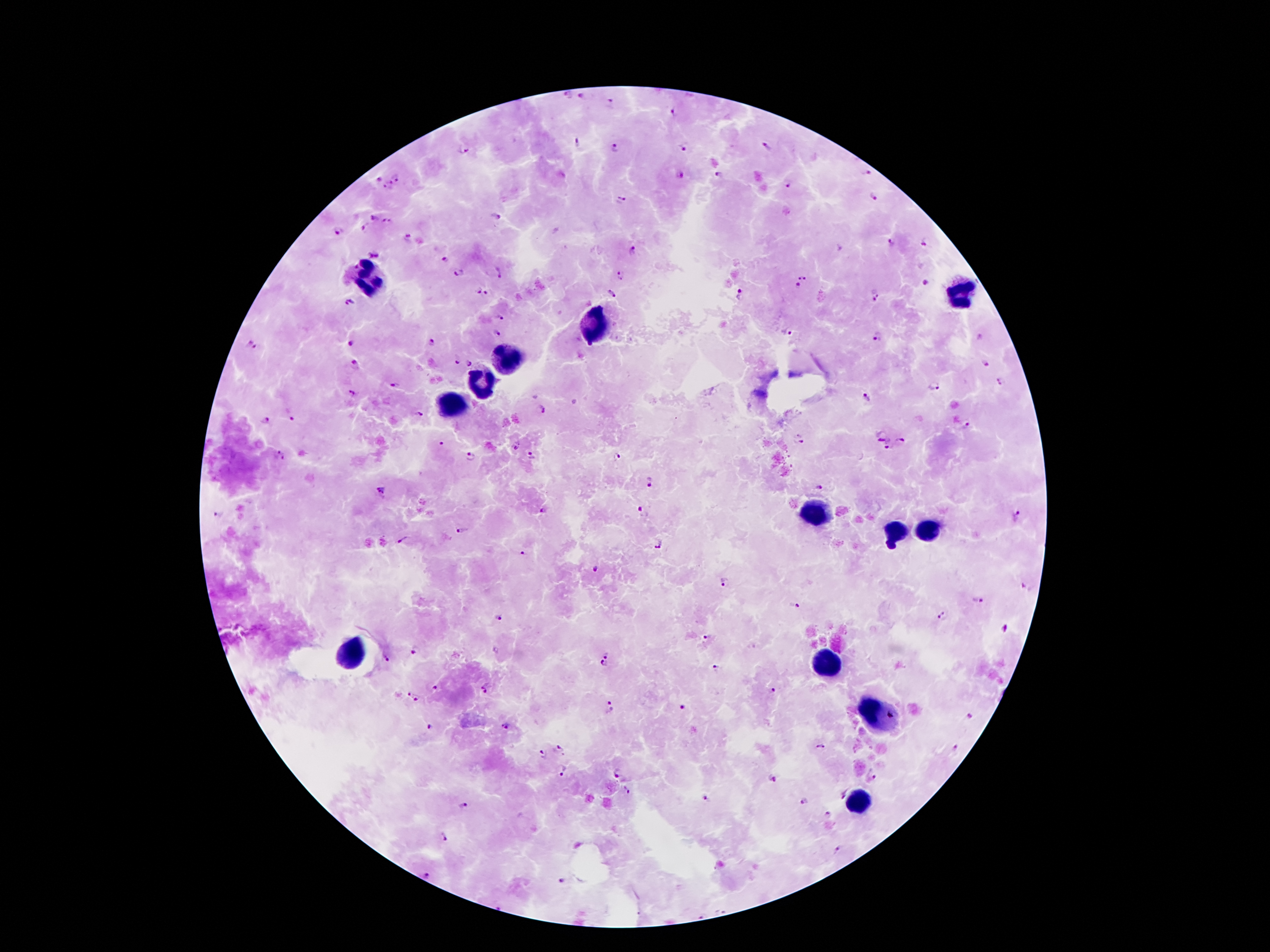 Approximate centers as [x, y] in pixels. Leukocyte locations: [372, 280], [960, 294], [592, 324], [508, 358], [480, 386], [450, 405], [816, 510], [895, 532], [932, 532], [347, 652], [829, 665], [876, 712], [859, 801]. Plasmodium parasite locations: [566, 96], [581, 97], [611, 104], [675, 114], [578, 143], [765, 146], [684, 147], [462, 149], [614, 150], [719, 173], [867, 173], [677, 176], [396, 178], [378, 179], [389, 183], [787, 185], [383, 188], [875, 197], [620, 201], [495, 217], [373, 218], [387, 221], [366, 229], [338, 231], [406, 239], [892, 243], [923, 243], [634, 249], [375, 256], [446, 261], [459, 271], [499, 271], [622, 275], [805, 276], [926, 282], [797, 284], [479, 291], [612, 292], [488, 293], [739, 293], [876, 297], [349, 303], [500, 317], [496, 332], [787, 332], [876, 335], [979, 338], [432, 341], [247, 342], [351, 343], [257, 348], [457, 359], [470, 363], [355, 364], [985, 364], [999, 381], [395, 386], [934, 386], [350, 393], [865, 397], [538, 409], [419, 414], [293, 419], [265, 420], [967, 423], [881, 435], [797, 438], [902, 440], [441, 445], [516, 446], [887, 447], [278, 450], [472, 455], [616, 456], [531, 457], [284, 458], [651, 480], [820, 487], [381, 490], [641, 509], [545, 510], [220, 514], [1015, 516], [465, 531], [403, 540], [660, 545], [523, 553], [596, 569], [726, 582], [1026, 588], [978, 599], [794, 606], [942, 615], [501, 618], [1005, 628], [706, 638], [415, 650], [608, 654], [386, 659], [605, 666], [717, 667], [437, 688], [487, 689], [774, 690], [410, 693], [417, 699], [611, 707], [681, 707], [969, 717], [430, 726], [505, 726], [821, 747], [954, 747], [559, 750], [542, 755], [562, 770], [618, 773], [874, 776], [772, 779], [627, 790], [840, 791], [705, 799], [805, 800], [464, 805], [828, 814], [443, 837], [840, 848], [425, 874], [562, 881]. Smartphone photograph taken through the microscope eyepiece. Thick peripheral-blood smear. Image is 1270×952 pixels. Giemsa stain. Patient malaria status: infected with Plasmodium falciparum. 100x magnification. Single field of view.